Point out each Plasmodium parasite.
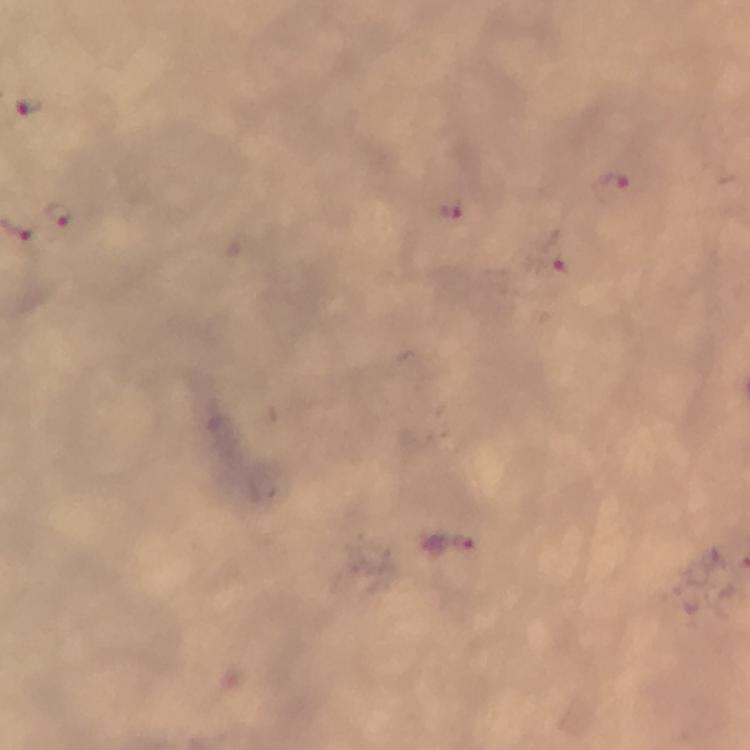
Approximate object centers, in pixels from the top-left corner.
Plasmodium parasites: (x=27, y=105), (x=613, y=183), (x=450, y=209), (x=60, y=213), (x=551, y=261), (x=449, y=550).

{
  "immersion_oil": "applied",
  "preparation": "thick blood smear",
  "image_size": "750×750 pixels",
  "capture": "smartphone mounted on the microscope",
  "cropped_from": "one field of view",
  "context": "from a malaria diagnostic workup",
  "magnification": "100x",
  "stain": "Giemsa"
}